Name the blood parasite species.
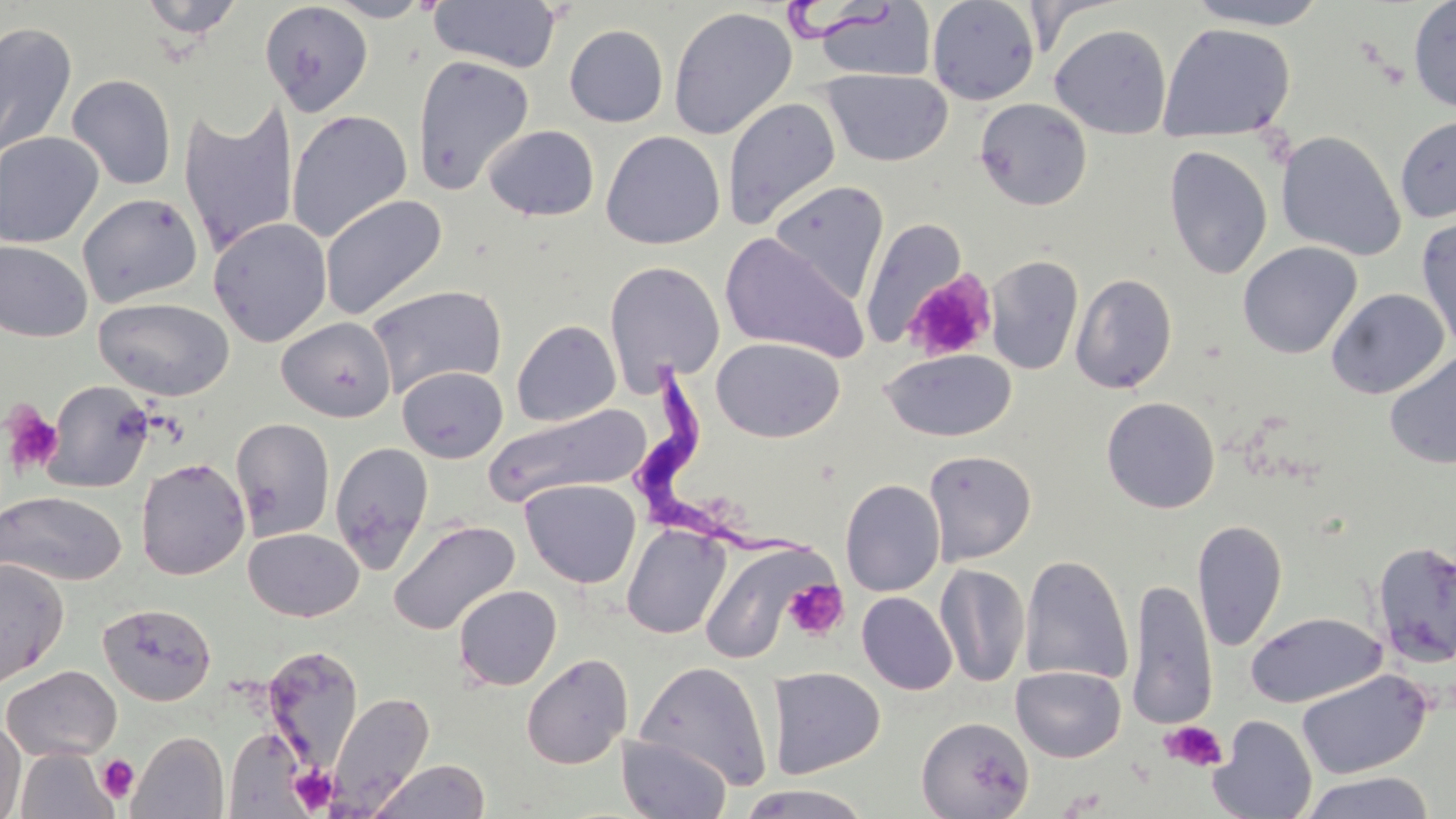
Trypanosoma brucei.

Summary:
  - Coordinate format: approximate bounding boxes as (x1, y1, x2, y2) in pixels
  - Platelet locations: (2, 404, 64, 476), (782, 578, 848, 640), (1159, 719, 1227, 772), (97, 754, 140, 803), (289, 764, 340, 814)
  - Trypanosoma brucei locations: (787, 0, 893, 42), (629, 364, 822, 572)
  - Uninfected red blood cell locations: (137, 0, 247, 39), (323, 0, 436, 21), (926, 0, 1041, 106), (1182, 0, 1335, 30), (1407, 0, 1456, 112), (428, 1, 563, 73), (259, 2, 374, 116), (811, 3, 937, 82), (668, 6, 797, 140), (1, 21, 78, 159), (1158, 23, 1295, 144), (564, 24, 669, 127), (1049, 24, 1172, 139), (412, 54, 535, 196), (821, 68, 954, 167), (67, 74, 177, 190), (722, 96, 841, 230), (177, 97, 299, 258), (974, 98, 1092, 211), (286, 109, 413, 242), (1395, 114, 1456, 224), (483, 125, 599, 221), (1276, 130, 1406, 261), (0, 131, 104, 248), (601, 131, 725, 250), (1163, 144, 1273, 280), (768, 180, 889, 302), (78, 192, 203, 307), (320, 194, 447, 320), (1416, 214, 1456, 354), (208, 217, 332, 347), (860, 217, 967, 346), (720, 233, 868, 362), (0, 241, 93, 342), (1237, 241, 1362, 359), (984, 255, 1084, 375), (604, 261, 725, 392), (902, 271, 999, 364), (1070, 272, 1178, 395), (366, 284, 507, 398), (1326, 288, 1450, 399), (93, 297, 234, 401), (276, 317, 396, 422), (511, 319, 621, 427), (712, 337, 845, 442), (880, 349, 1016, 442), (1384, 352, 1456, 470), (397, 366, 508, 463), (42, 380, 155, 493), (1100, 396, 1220, 513), (482, 404, 652, 507), (231, 418, 335, 541), (330, 441, 434, 573), (923, 450, 1036, 564), (135, 458, 251, 580), (521, 479, 641, 588), (840, 479, 946, 597), (0, 490, 126, 586), (388, 519, 520, 635), (1192, 519, 1287, 652), (621, 523, 731, 640), (244, 528, 363, 622), (1373, 539, 1456, 668), (701, 541, 825, 664), (1019, 555, 1134, 686), (0, 558, 69, 688), (934, 563, 1030, 687), (1127, 578, 1218, 729), (453, 584, 562, 690), (856, 591, 958, 695), (97, 602, 217, 706), (1246, 611, 1386, 708), (262, 646, 365, 771), (520, 653, 633, 770), (635, 660, 773, 790), (1, 665, 122, 761), (1011, 665, 1126, 762), (767, 667, 885, 779), (1296, 669, 1433, 779), (327, 691, 435, 812), (1209, 714, 1317, 819), (916, 716, 1034, 818), (0, 719, 26, 819), (224, 728, 309, 815), (128, 731, 229, 819), (616, 735, 732, 818), (15, 747, 119, 818), (367, 759, 491, 819), (1299, 770, 1435, 819), (735, 783, 876, 818)
  - Stain: May-Grünwald-Giemsa
  - Magnification: 1000x
  - Field of view: single
  - Modality: light microscopy
  - Preparation: thin blood film
  - Image size: 1456×819 pixels